Outline each Plasmodium falciparum-infected red blood cell.
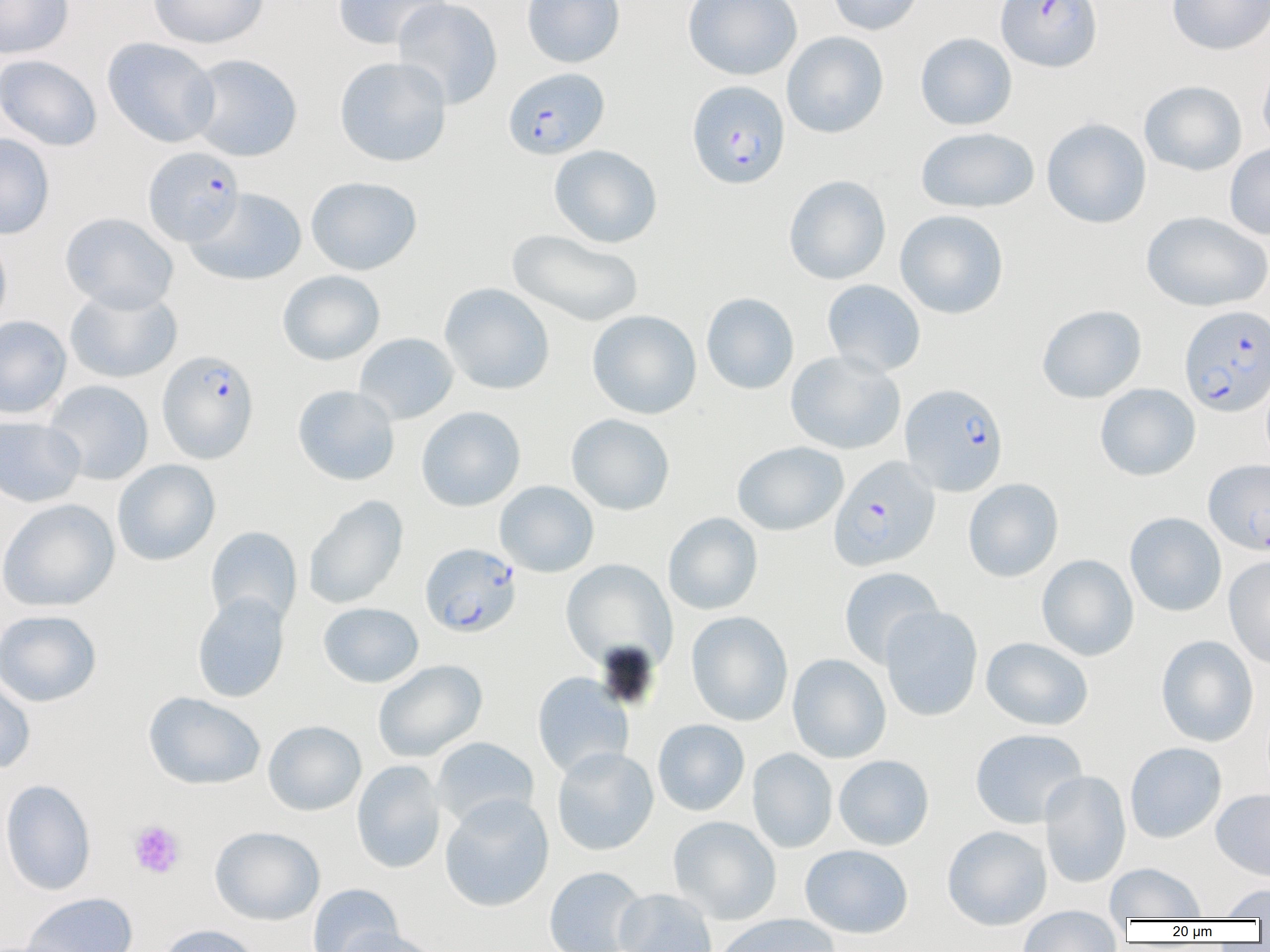
Approximate bounding boxes as (x1, y1, x2, y2) in pixels.
Plasmodium falciparum-infected red blood cells: (995, 0, 1102, 72), (503, 67, 609, 159), (687, 80, 790, 190), (143, 146, 245, 246), (1179, 304, 1269, 417), (157, 349, 259, 464), (900, 382, 1009, 496), (829, 456, 941, 571), (420, 543, 522, 637).

Summary:
  - Platelet locations: (128, 820, 186, 879)
  - Uninfected red blood cell locations: (0, 0, 74, 59), (148, 0, 269, 49), (332, 0, 452, 51), (392, 0, 503, 109), (521, 0, 625, 68), (682, 0, 803, 80), (827, 0, 924, 35), (1167, 0, 1270, 55), (782, 31, 889, 138), (915, 32, 1017, 130), (102, 37, 220, 148), (186, 53, 303, 162), (0, 54, 102, 151), (334, 56, 452, 167), (1257, 57, 1270, 153), (1139, 80, 1247, 176), (1041, 118, 1152, 229), (916, 126, 1040, 213), (0, 133, 55, 239), (1225, 142, 1270, 240), (549, 144, 663, 248), (783, 175, 891, 285), (305, 176, 422, 275), (186, 187, 307, 286), (895, 209, 1009, 320), (1141, 211, 1270, 312), (60, 212, 179, 312), (507, 230, 644, 328), (0, 233, 12, 333), (277, 270, 385, 365), (822, 279, 926, 377), (439, 283, 555, 395), (65, 286, 182, 384), (701, 292, 799, 394), (1036, 304, 1147, 404), (587, 309, 702, 419), (0, 315, 71, 419), (354, 333, 459, 425), (785, 350, 906, 455), (43, 380, 154, 485), (1095, 383, 1200, 481), (292, 384, 400, 486), (416, 406, 526, 512), (566, 413, 675, 515), (0, 415, 86, 508), (733, 441, 848, 536), (1203, 458, 1269, 554), (112, 459, 220, 566), (963, 478, 1063, 582), (494, 481, 599, 577), (304, 494, 409, 610), (0, 498, 119, 612), (663, 512, 763, 615), (1125, 512, 1227, 617), (205, 526, 302, 628), (1037, 554, 1139, 661), (1223, 556, 1270, 669), (561, 559, 677, 671), (838, 566, 944, 669), (192, 592, 290, 703), (318, 602, 424, 687), (880, 606, 983, 721), (0, 609, 102, 707), (686, 611, 793, 726), (1156, 635, 1259, 747), (981, 637, 1093, 731), (787, 654, 891, 763), (372, 659, 487, 762), (532, 672, 634, 779), (0, 675, 36, 774), (143, 691, 265, 791), (652, 719, 750, 816), (263, 720, 366, 816), (970, 728, 1088, 829), (431, 737, 539, 829), (1124, 742, 1226, 843), (552, 746, 659, 856), (747, 748, 837, 853), (834, 755, 934, 850), (351, 760, 446, 874), (1039, 770, 1131, 888), (1, 778, 97, 896), (1211, 788, 1270, 881), (439, 793, 554, 912), (668, 816, 782, 924), (942, 825, 1052, 930), (210, 826, 325, 925), (799, 844, 913, 938), (1105, 862, 1207, 920), (543, 866, 647, 952), (307, 883, 404, 952), (1217, 883, 1270, 919), (614, 888, 717, 952), (22, 892, 138, 952), (1018, 907, 1123, 952), (713, 914, 840, 952), (157, 924, 263, 952), (333, 927, 445, 952)
  - Slide-level diagnosis: Plasmodium falciparum
  - Magnification: 1000x
  - Field of view: one of a larger specimen
  - Modality: light microscopy
  - Preparation: thin blood smear
  - Image size: 1270×952 pixels